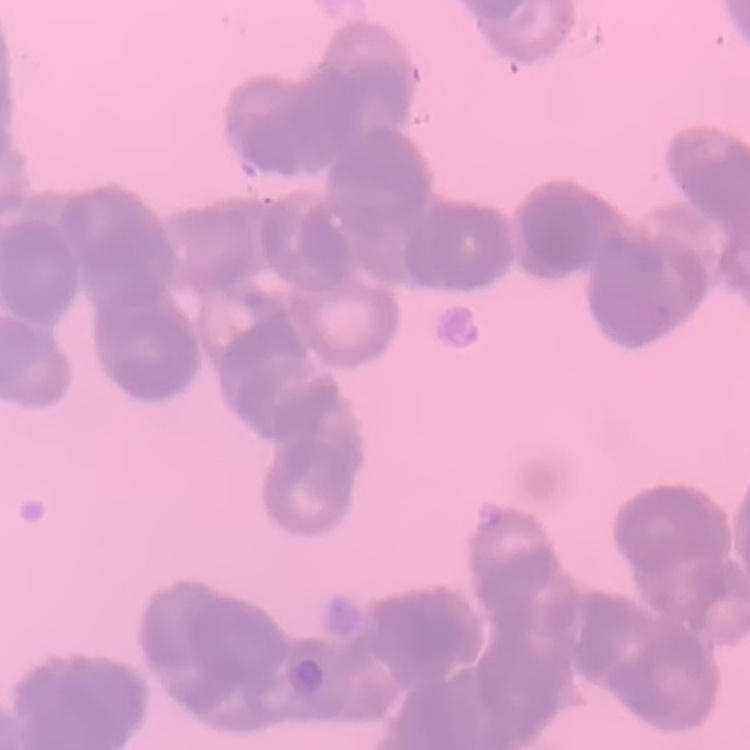
The red blood cells exhibit rouleaux formation. Thin blood film. Square crop of a larger photomicrograph. Field's or Giemsa stain.